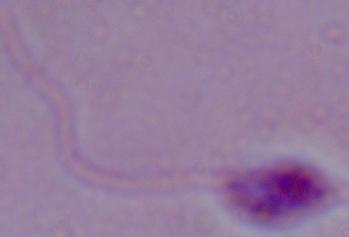
1000x magnification. A Leishmania parasite is shown. Micrograph.